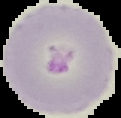

{
  "image_size": "121×118 pixels",
  "malaria_status": "parasitized",
  "preparation": "thin blood film",
  "image_type": "segmented cell region on a black background"
}